Report the malaria status of this cell.
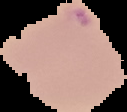
It is parasitized.

Summary:
  - Image type: cell region segmented out of the field of view; surrounding area masked to black
  - Preparation: thin blood film
  - Image size: 127×112 pixels